Assess the morphology of the erythrocytes.
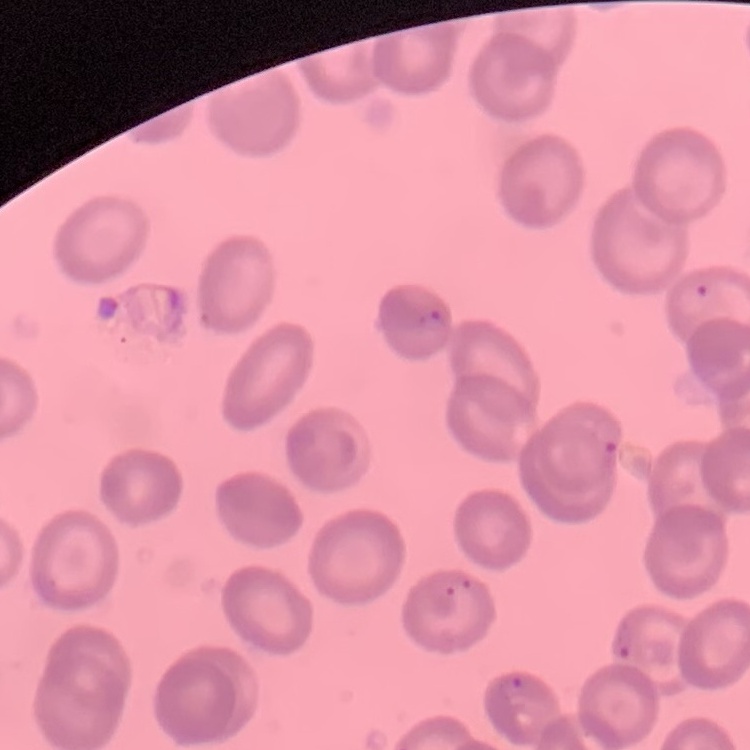
They show no rouleaux formation.

Summary:
  - Image type: one tile cut from a larger photomicrograph
  - Preparation: thin blood smear
  - Stain: Field's or Giemsa